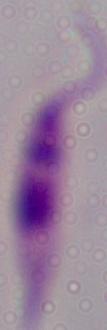

Summary:
  - Magnification: 1000x
  - Modality: photomicrograph
  - Identification: Leishmania